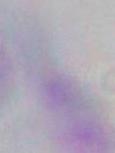

Toxoplasma gondii is shown. Captured at 1000x magnification. Micrograph.